Outline each Plasmodium malariae-infected red blood cell.
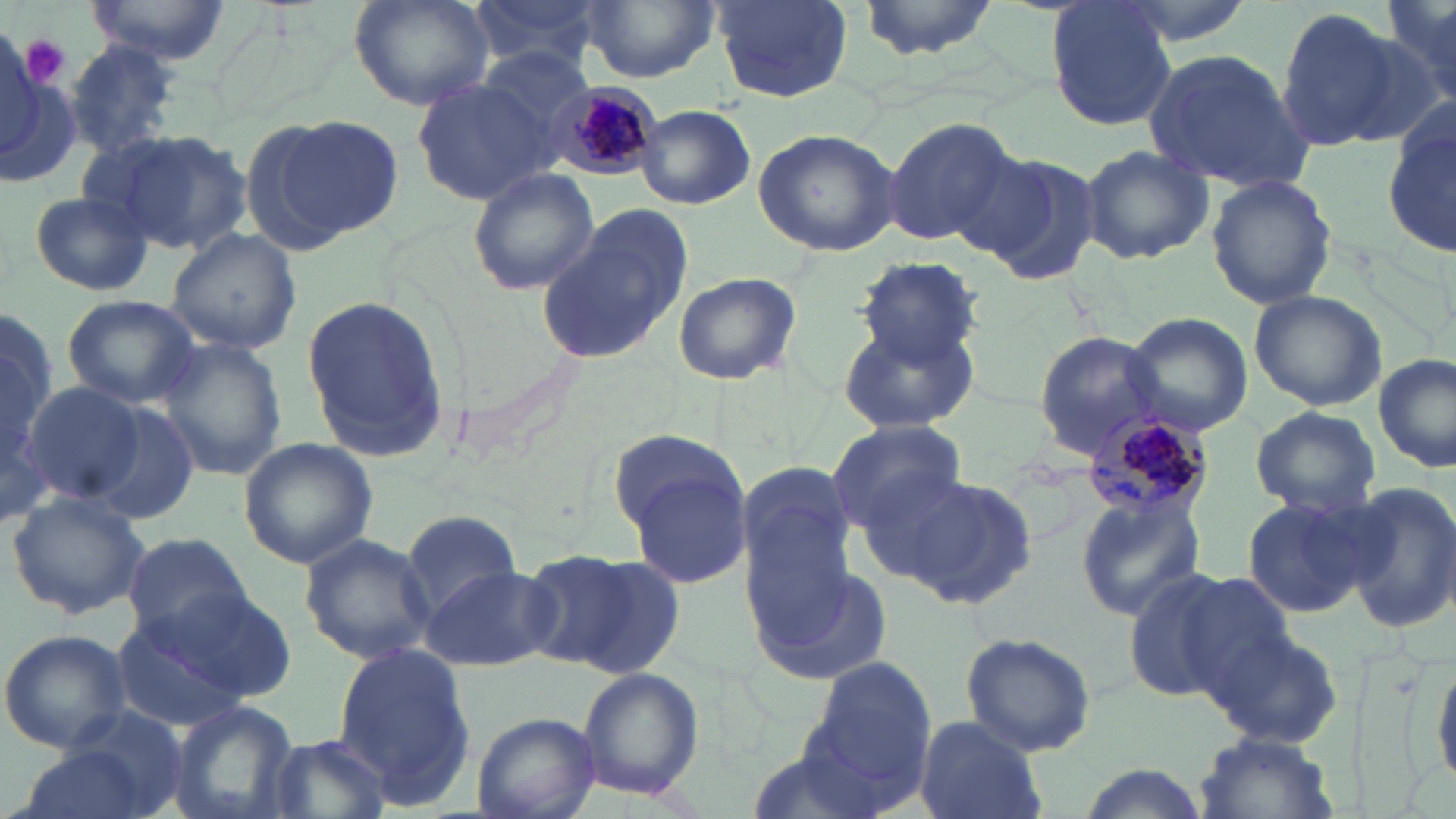

Approximate bounding boxes as (x1, y1, x2, y2) in pixels.
Plasmodium malariae-infected red blood cells: (550, 82, 661, 178), (1085, 407, 1216, 521).

{
  "slide_level_diagnosis": "Plasmodium malariae",
  "uninfected_red_blood_cell_locations": "approximate bounding boxes as (x1, y1, x2, y2) in pixels: (84, 0, 231, 63), (351, 0, 496, 111), (469, 0, 609, 77), (578, 0, 722, 83), (709, 0, 854, 103), (857, 0, 1000, 57), (1047, 0, 1177, 131), (1108, 0, 1258, 50), (1381, 2, 1456, 98), (1275, 7, 1400, 151), (1341, 23, 1451, 147), (63, 39, 184, 158), (478, 47, 596, 143), (1141, 47, 1311, 191), (0, 67, 81, 188), (413, 76, 556, 206), (1385, 95, 1456, 261), (635, 104, 755, 210), (242, 114, 394, 253), (880, 118, 1016, 246), (753, 128, 901, 256), (103, 130, 251, 256), (1079, 143, 1214, 266), (968, 149, 1104, 286), (468, 168, 598, 296), (1207, 172, 1337, 308), (29, 191, 155, 297), (536, 208, 692, 366), (167, 227, 302, 355), (851, 256, 984, 370), (672, 271, 801, 387), (1247, 288, 1388, 411), (300, 292, 448, 463), (62, 294, 201, 407), (1124, 312, 1252, 436), (837, 320, 977, 435), (1032, 331, 1169, 459), (157, 338, 289, 480), (1376, 352, 1455, 475), (23, 383, 147, 506), (72, 395, 201, 526), (1249, 406, 1383, 517), (828, 419, 966, 532), (609, 430, 744, 538), (239, 437, 377, 570), (623, 456, 754, 594), (733, 459, 861, 606), (852, 466, 990, 585), (896, 474, 1041, 611), (1343, 482, 1456, 633), (5, 490, 151, 619), (1073, 491, 1206, 621), (1242, 491, 1381, 616), (401, 510, 525, 614), (122, 532, 252, 643), (300, 533, 442, 664), (746, 543, 893, 689), (522, 549, 678, 677), (420, 563, 557, 672), (1119, 565, 1259, 705), (131, 587, 297, 713), (1205, 625, 1345, 750), (0, 628, 132, 754), (958, 631, 1098, 757), (331, 642, 476, 804), (1427, 649, 1456, 791), (805, 655, 938, 794), (578, 667, 703, 801), (169, 700, 300, 819), (473, 711, 599, 819), (914, 716, 1047, 819), (1191, 731, 1341, 819), (263, 733, 390, 819), (746, 737, 903, 819), (15, 742, 157, 819), (1071, 764, 1213, 819)",
  "image_size": "1456×819 pixels",
  "stain": "May-Grünwald-Giemsa",
  "magnification": "1000x",
  "platelet_locations": "approximate bounding boxes as (x1, y1, x2, y2) in pixels: (18, 34, 70, 88)",
  "modality": "optical microscopy",
  "field_of_view": "single",
  "preparation": "thin blood smear"
}